Classify this cell by malaria status.
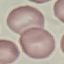
Uninfected.

{
  "image_type": "cell patch, automatically extracted from a larger field of view and resized to 64 × 64 pixels",
  "stain": "Giemsa",
  "preparation": "thin blood smear",
  "capture": "smartphone through the microscope eyepiece"
}